Point out each malaria parasite.
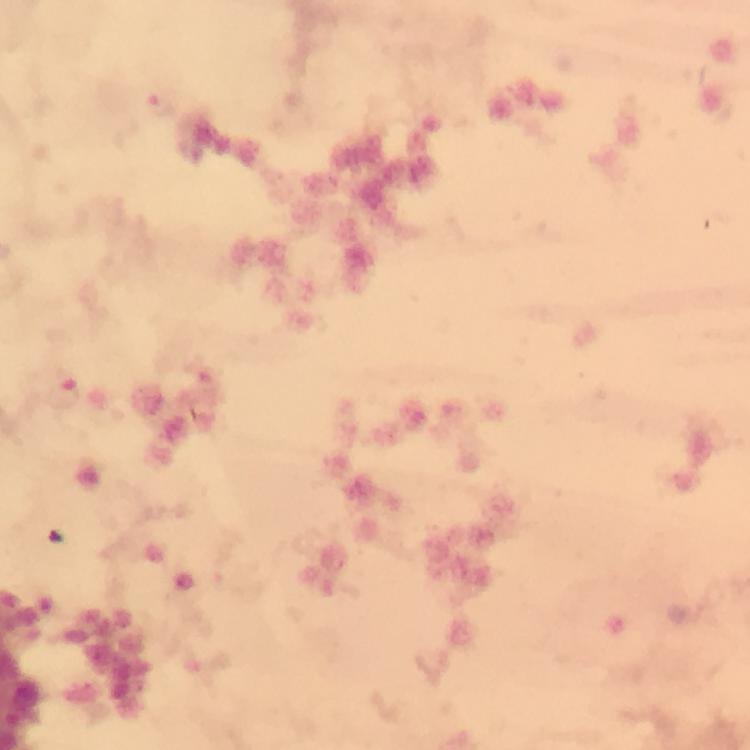

Approximate centers as (x, y) in pixels.
Malaria parasites: (161, 107), (64, 396).

Summary:
  - Image size: 750×750 pixels
  - Immersion oil: used
  - Stain: Giemsa
  - Context: from a malaria diagnostic workup
  - Cropped from: a single field of view
  - Magnification: 100x
  - Capture: smartphone camera through the microscope
  - Preparation: thick blood smear